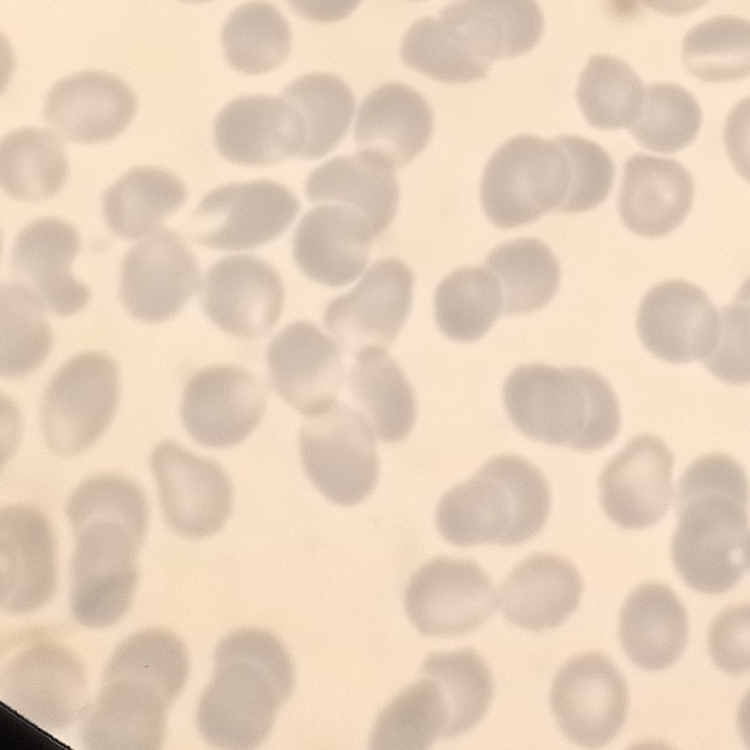 The red blood cells show no rouleaux formation. One tile cut from a larger photomicrograph. Thin blood film. Field's or Giemsa stain.